Identify the parasite.
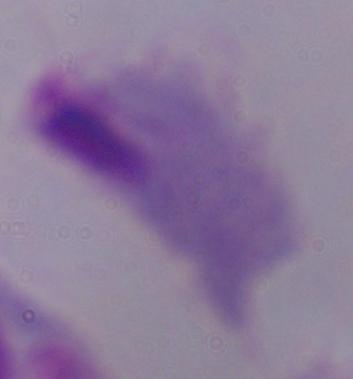

This is a trichomonad.

{
  "magnification": "1000x",
  "modality": "micrograph"
}